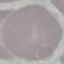 Malaria status: uninfected. Acquired by smartphone through the microscope eyepiece. Thin blood smear. Giemsa-stained preparation. Automatically extracted cell patch, resized to 64 × 64 pixels.